Assess this cell for malaria.
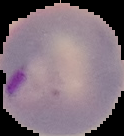

Parasitized.

image type = segmented cell region with the area outside set to black
preparation = thin blood smear
image size = 124×136 pixels